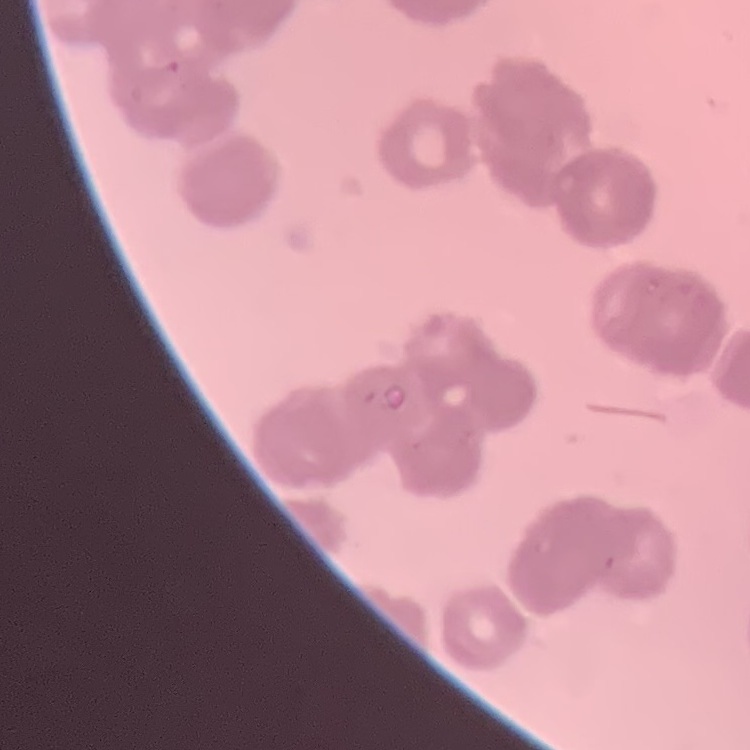

red blood cell morphology = rouleaux formation
preparation = thin blood smear
image type = one tile cut from a larger photomicrograph
stain = Field's or Giemsa